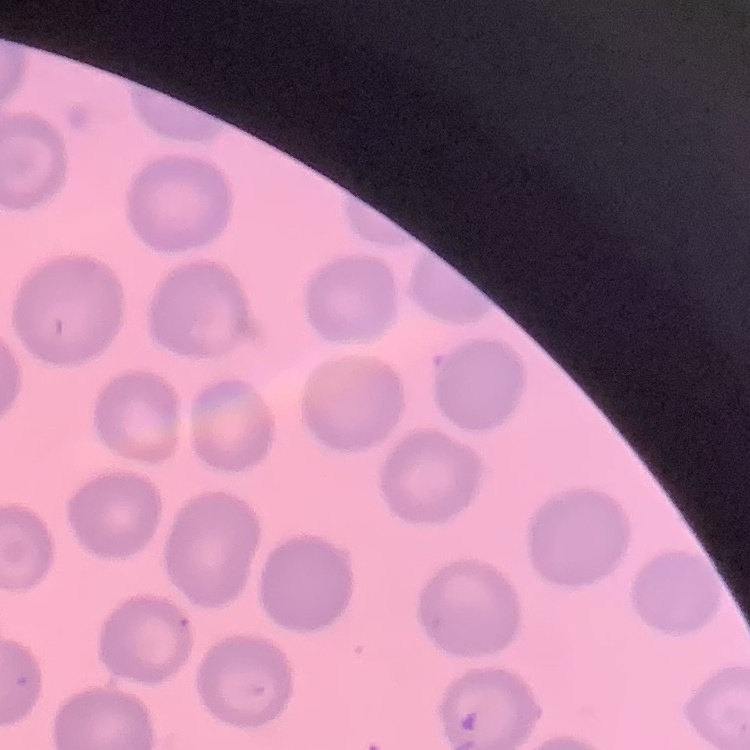

Summary:
  - Erythrocyte morphology: no rouleaux formation
  - Image type: one tile cut from a larger photomicrograph
  - Preparation: thin peripheral smear
  - Stain: Field's or Giemsa